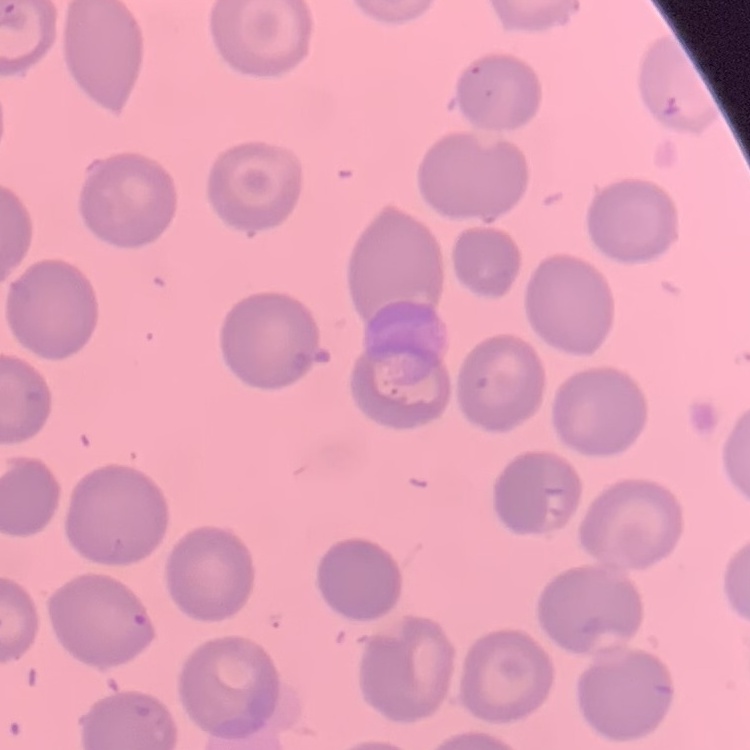
Summary:
  - Red blood cell morphology: no rouleaux formation
  - Stain: Field's or Giemsa
  - Preparation: thin blood film
  - Image type: square crop of a larger photomicrograph